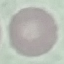
malaria status = uninfected
capture = smartphone camera at the microscope eyepiece
image type = automatically extracted cell patch, resized to 64 × 64 pixels
stain = Giemsa
preparation = thin blood film